Outline each blood parasite and name the species.
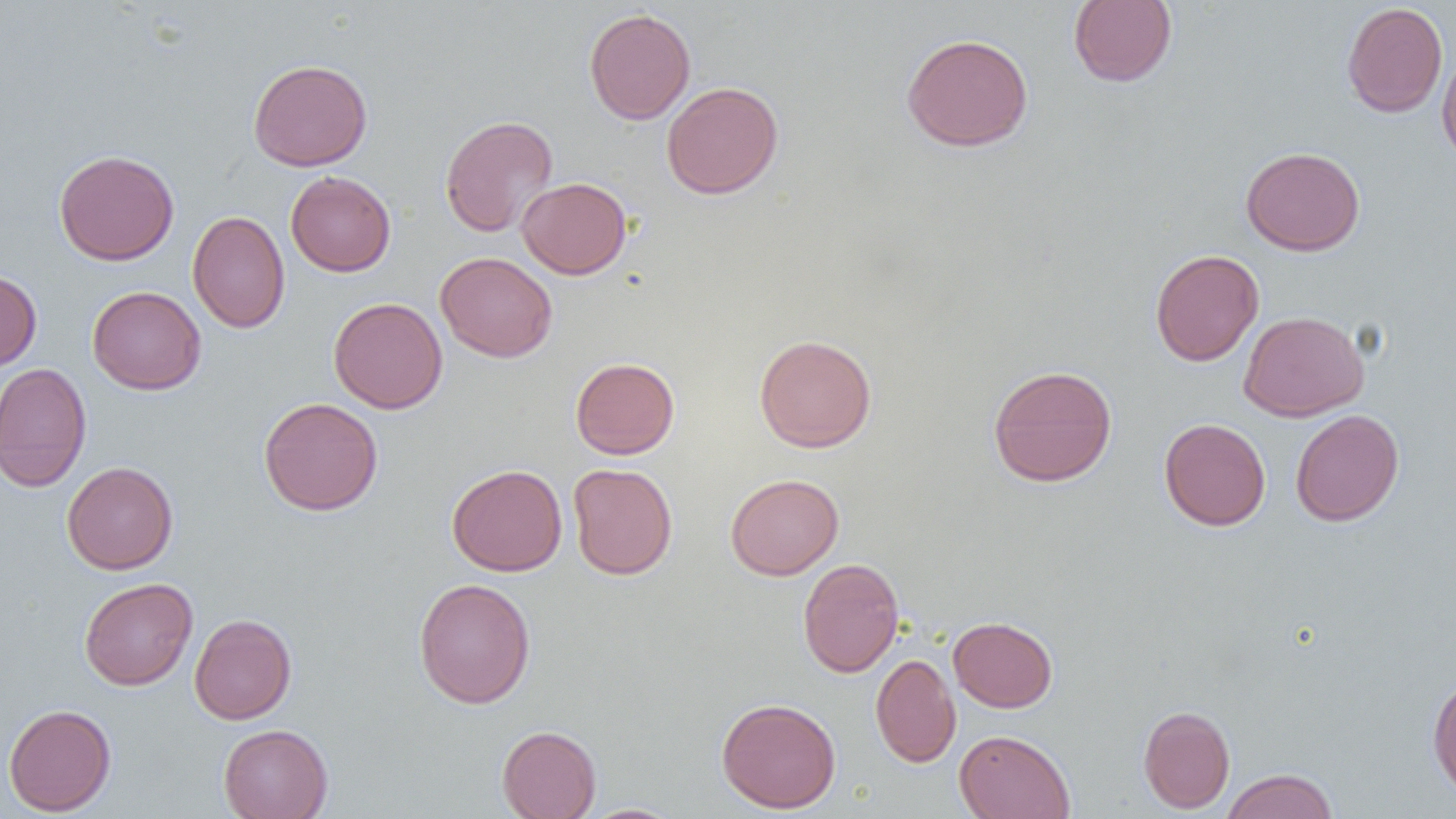

No blood parasites seen.

slide-level diagnosis = no evidence of blood parasites
modality = light microscopy
preparation = thin blood film
field of view = single
uninfected red blood cell locations = approximate bounding boxes as (x1,y1)-(x2,y2) corner pairs in pixels: (1068,0)-(1177,87), (1341,2)-(1448,118), (584,8)-(696,125), (901,33)-(1034,152), (1436,46)-(1456,166), (247,58)-(373,171), (661,81)-(784,199), (440,114)-(558,237), (1240,146)-(1366,256), (54,150)-(180,266), (285,171)-(396,276), (517,177)-(632,279), (187,210)-(290,333), (1150,249)-(1264,366), (435,251)-(558,362), (0,269)-(42,371), (87,286)-(206,395), (328,297)-(447,414), (1239,311)-(1369,421), (754,334)-(877,453), (570,357)-(680,459), (0,362)-(92,492), (987,365)-(1117,487), (258,397)-(383,516), (1290,409)-(1404,526), (1159,418)-(1271,531), (62,461)-(178,574), (447,463)-(567,576), (568,463)-(678,579), (725,473)-(844,580), (797,558)-(904,678), (79,577)-(198,691), (413,577)-(536,709), (189,614)-(297,724), (948,616)-(1058,712), (871,653)-(961,768), (1427,675)-(1456,797), (716,697)-(841,813), (3,703)-(117,816), (1138,705)-(1235,813), (218,724)-(333,819), (496,725)-(602,819), (954,729)-(1075,819), (1221,768)-(1339,819), (577,803)-(687,819)
image size = 1456×819 pixels
magnification = 1000x